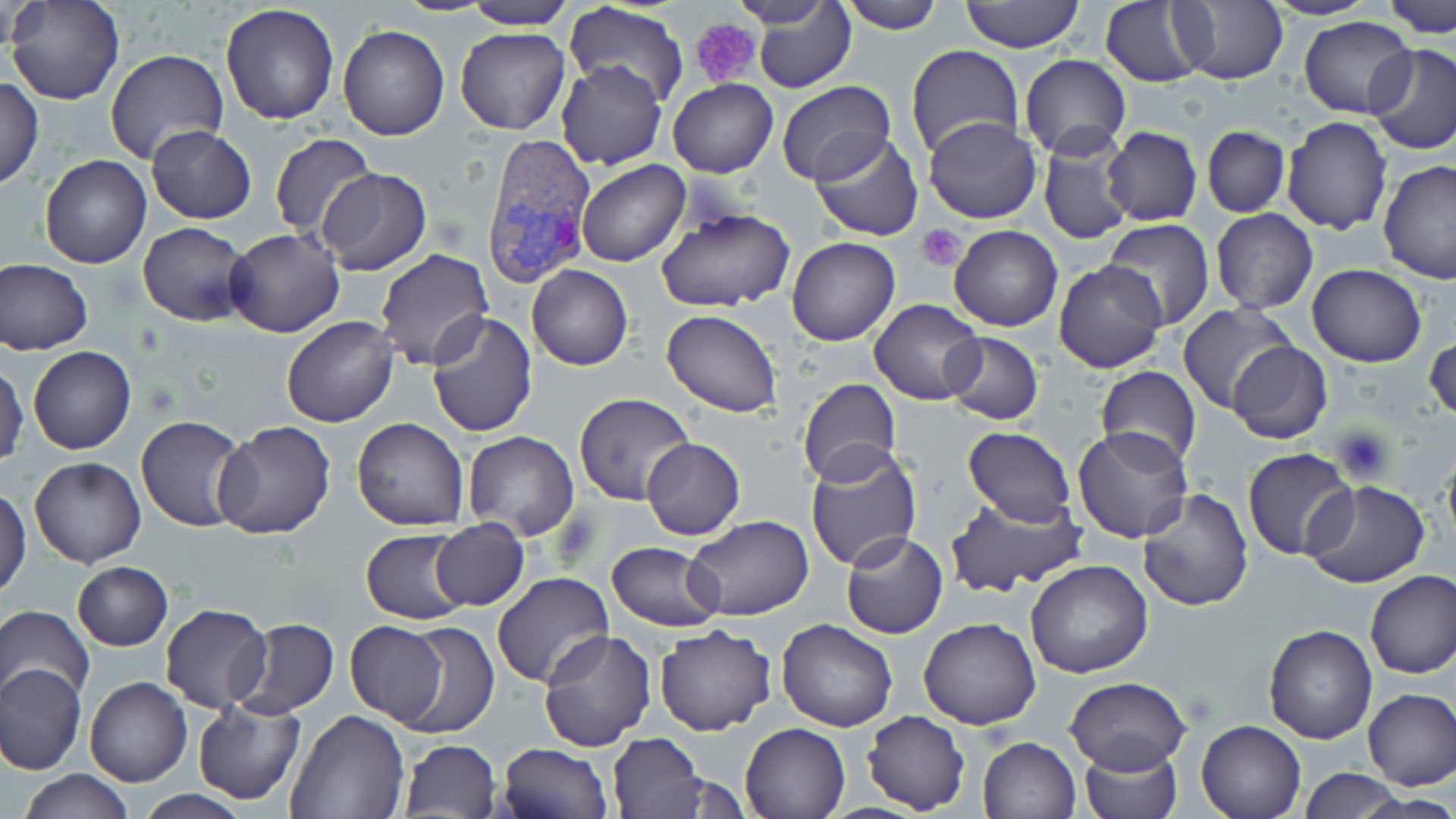

Approximate bounding boxes as [x1, y1, x2, y2] in pixels. Uninfected red blood cell locations: [6, 0, 126, 106], [392, 0, 496, 15], [728, 0, 838, 29], [839, 0, 943, 33], [1100, 0, 1209, 86], [1172, 0, 1289, 85], [1261, 0, 1378, 21], [1383, 0, 1456, 37], [959, 1, 1086, 51], [461, 2, 576, 30], [562, 2, 689, 108], [753, 3, 856, 93], [5, 4, 49, 51], [220, 4, 341, 125], [1299, 17, 1417, 118], [338, 25, 450, 142], [455, 27, 570, 135], [906, 44, 1024, 161], [1365, 44, 1456, 155], [104, 49, 230, 167], [1020, 54, 1131, 161], [556, 60, 666, 169], [0, 75, 43, 192], [668, 77, 777, 178], [773, 80, 896, 187], [924, 116, 1041, 224], [1282, 116, 1394, 235], [146, 125, 256, 223], [1202, 125, 1289, 218], [800, 126, 915, 341], [1102, 126, 1201, 227], [808, 132, 925, 241], [268, 134, 376, 241], [1038, 135, 1132, 246], [39, 155, 152, 270], [576, 159, 689, 267], [1376, 160, 1456, 286], [316, 168, 431, 275], [653, 207, 795, 313], [1210, 208, 1317, 313], [1102, 218, 1214, 328], [137, 221, 253, 326], [948, 225, 1063, 331], [224, 229, 345, 338], [786, 238, 900, 347], [373, 249, 493, 372], [1, 258, 93, 354], [1053, 259, 1168, 374], [1306, 262, 1427, 366], [527, 265, 633, 369], [869, 298, 984, 405], [1176, 303, 1299, 416], [663, 309, 782, 419], [425, 312, 539, 437], [281, 316, 398, 427], [1425, 330, 1455, 427], [942, 331, 1044, 424], [1227, 342, 1333, 445], [27, 345, 136, 455], [1, 358, 27, 470], [1097, 366, 1200, 469], [796, 378, 901, 488], [574, 392, 694, 504], [136, 415, 249, 531], [352, 417, 469, 531], [211, 422, 336, 539], [1072, 425, 1193, 542], [962, 429, 1075, 527], [462, 431, 579, 541], [641, 438, 746, 539], [803, 445, 923, 573], [1441, 445, 1456, 556], [1242, 448, 1358, 562], [647, 453, 767, 596], [29, 457, 145, 568], [1303, 480, 1431, 589], [0, 485, 31, 599], [1137, 486, 1253, 611], [942, 491, 1087, 598], [684, 514, 814, 620], [429, 518, 528, 610], [360, 529, 472, 625], [841, 531, 948, 639], [605, 541, 723, 632], [1025, 561, 1152, 679], [72, 562, 173, 651], [1366, 570, 1456, 678], [492, 572, 615, 690], [158, 604, 271, 713], [0, 606, 94, 708], [236, 618, 338, 717], [918, 618, 1042, 729], [392, 620, 499, 741], [777, 620, 898, 732], [344, 622, 451, 729], [654, 623, 776, 735], [1264, 625, 1377, 743], [537, 630, 656, 751], [0, 662, 86, 775], [84, 676, 193, 788], [1066, 676, 1191, 772], [1361, 688, 1456, 790], [191, 697, 305, 803], [285, 710, 411, 819], [861, 710, 971, 815], [1195, 719, 1307, 819], [739, 720, 853, 819], [605, 732, 709, 819], [977, 736, 1081, 819], [399, 738, 499, 819], [496, 742, 612, 819], [1078, 744, 1182, 819], [1298, 768, 1408, 818], [19, 770, 133, 817]. Plasmodium vivax-infected red blood cell locations: [479, 132, 595, 290]. Platelet locations: [692, 19, 761, 89], [917, 224, 967, 271]. Slide-level diagnosis: Plasmodium vivax. May-Grünwald-Giemsa-stained preparation. Thin blood film. One field of a larger specimen. Captured at 1000x magnification. Image is 1456×819 pixels. Light microscopy.